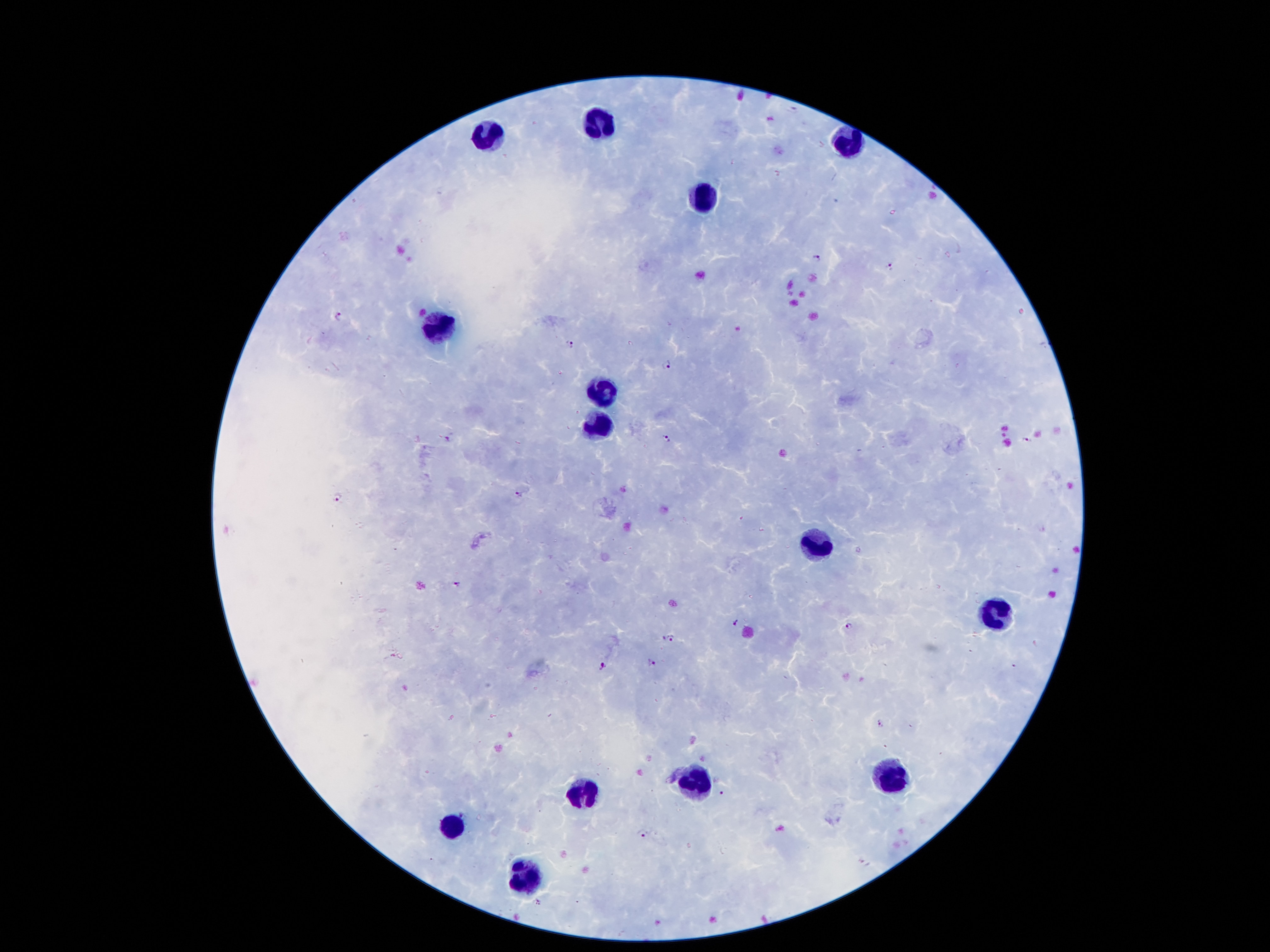

Approximate centers as (x, y) in pixels. Leukocyte locations: (598, 125), (490, 134), (850, 141), (706, 196), (441, 324), (601, 389), (601, 428), (813, 548), (994, 614), (890, 778), (693, 782), (581, 791), (452, 826), (523, 877). Plasmodium parasite locations: (819, 259), (889, 269), (339, 316), (569, 344), (667, 364), (667, 437), (448, 439), (1026, 440), (520, 493), (338, 499), (455, 585), (733, 623), (850, 626), (670, 639), (652, 663), (605, 665), (880, 725), (722, 794), (642, 833). Image is 1270×952 pixels. Single field of view. Giemsa stain. 100x magnification. Thick peripheral-blood smear. Photographed through the microscope eyepiece with a smartphone camera. Patient malaria status: positive for Plasmodium falciparum.